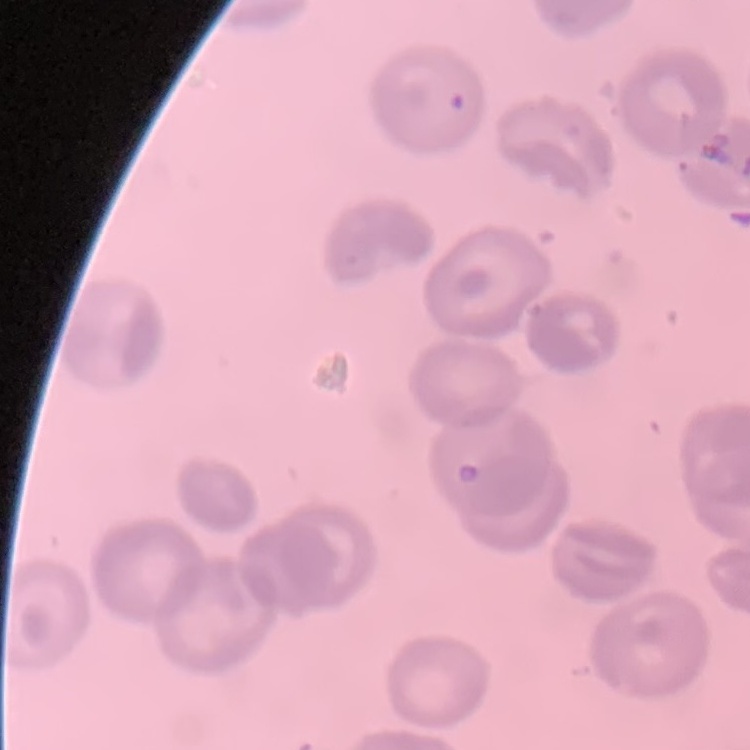

The red blood cells exhibit no rouleaux formation. Stained with either Field's or Giemsa. Thin peripheral smear. One tile cut from a larger photomicrograph.